Assess for Plasmodium parasites.
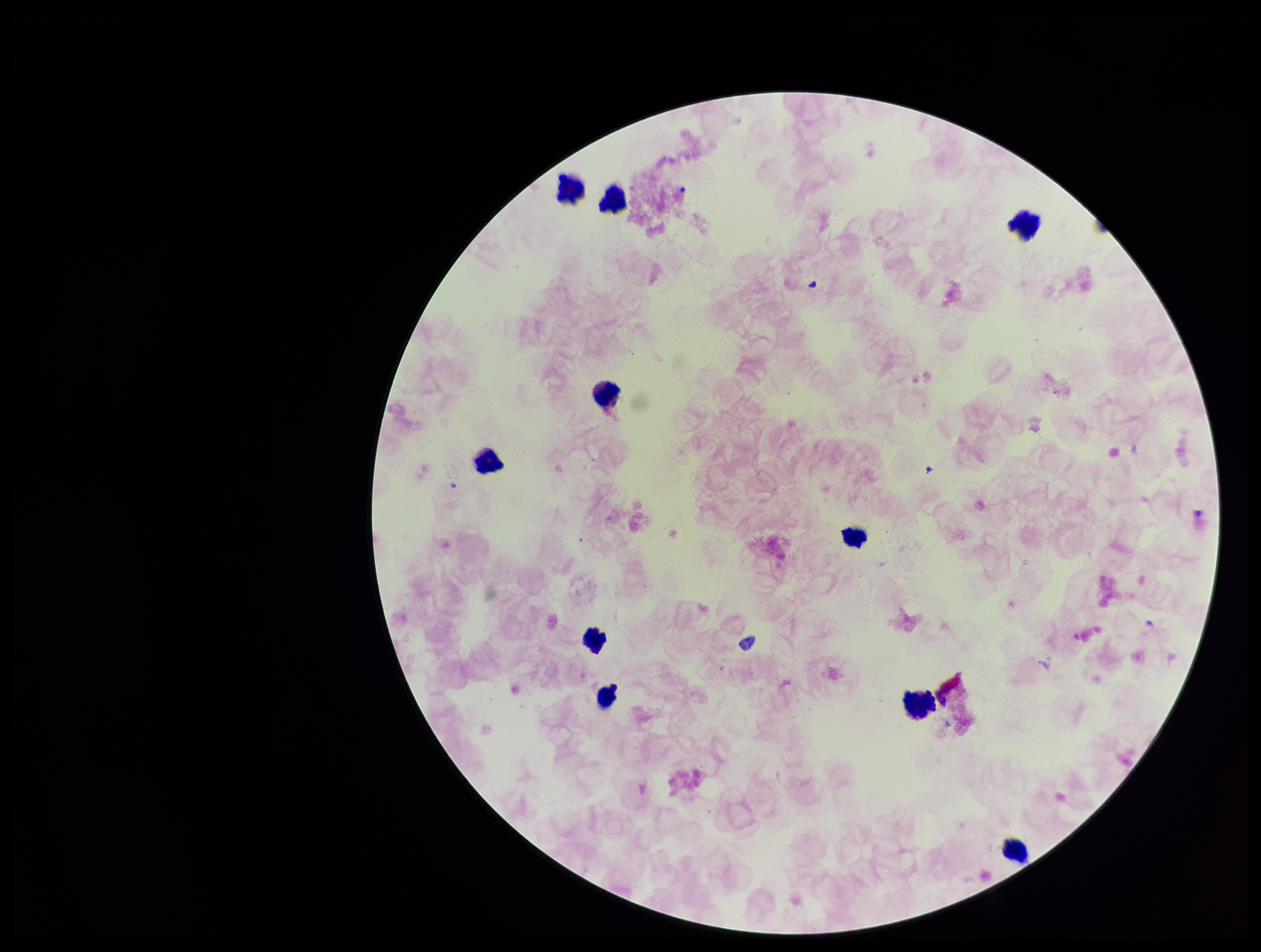

None detected.

preparation = thick blood smear
patient malaria status = negative
capture = smartphone photograph through the microscope eyepiece
image size = 1261×952 pixels
field of view = one from this slide
leukocyte count = 10
parasite count = 0
stain = Giemsa